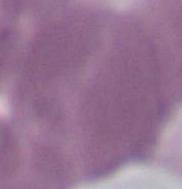

{
  "identification": "erythrocyte",
  "magnification": "1000x",
  "modality": "photomicrograph"
}